Report the malaria status of this cell.
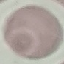
Uninfected.

Thin smear of blood. Photographed with a smartphone camera at the microscope eyepiece. Giemsa-stained preparation. Automatically extracted cell patch, resized to 64 × 64 pixels.